Comment on the morphology of the red blood cells.
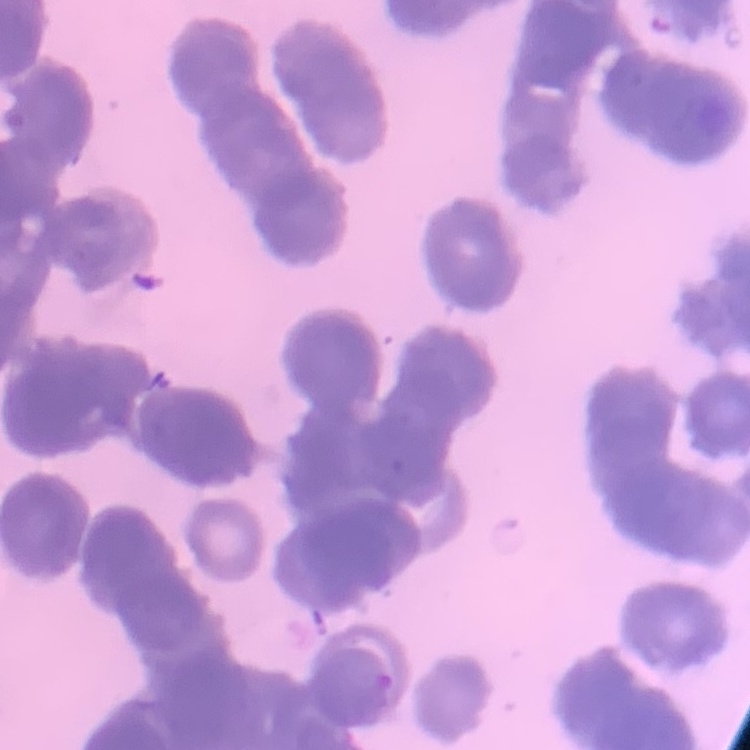

They show rouleaux formation.

One tile cut from a larger photomicrograph. Stained with either Field's or Giemsa. Thin blood smear.